Describe the morphology of the erythrocytes.
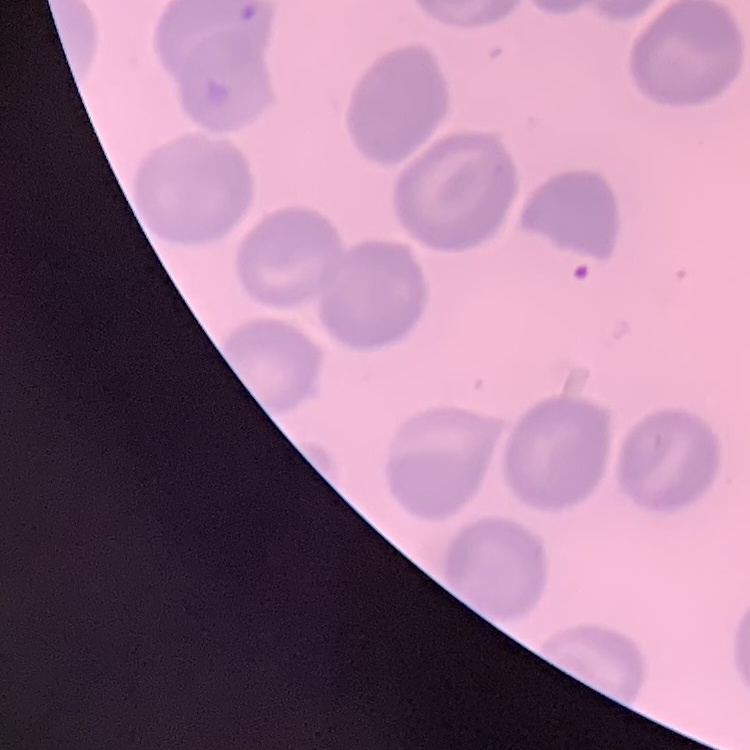

No rouleaux formation.

Thin blood smear. Square crop of a larger photomicrograph. Field's or Giemsa stain.